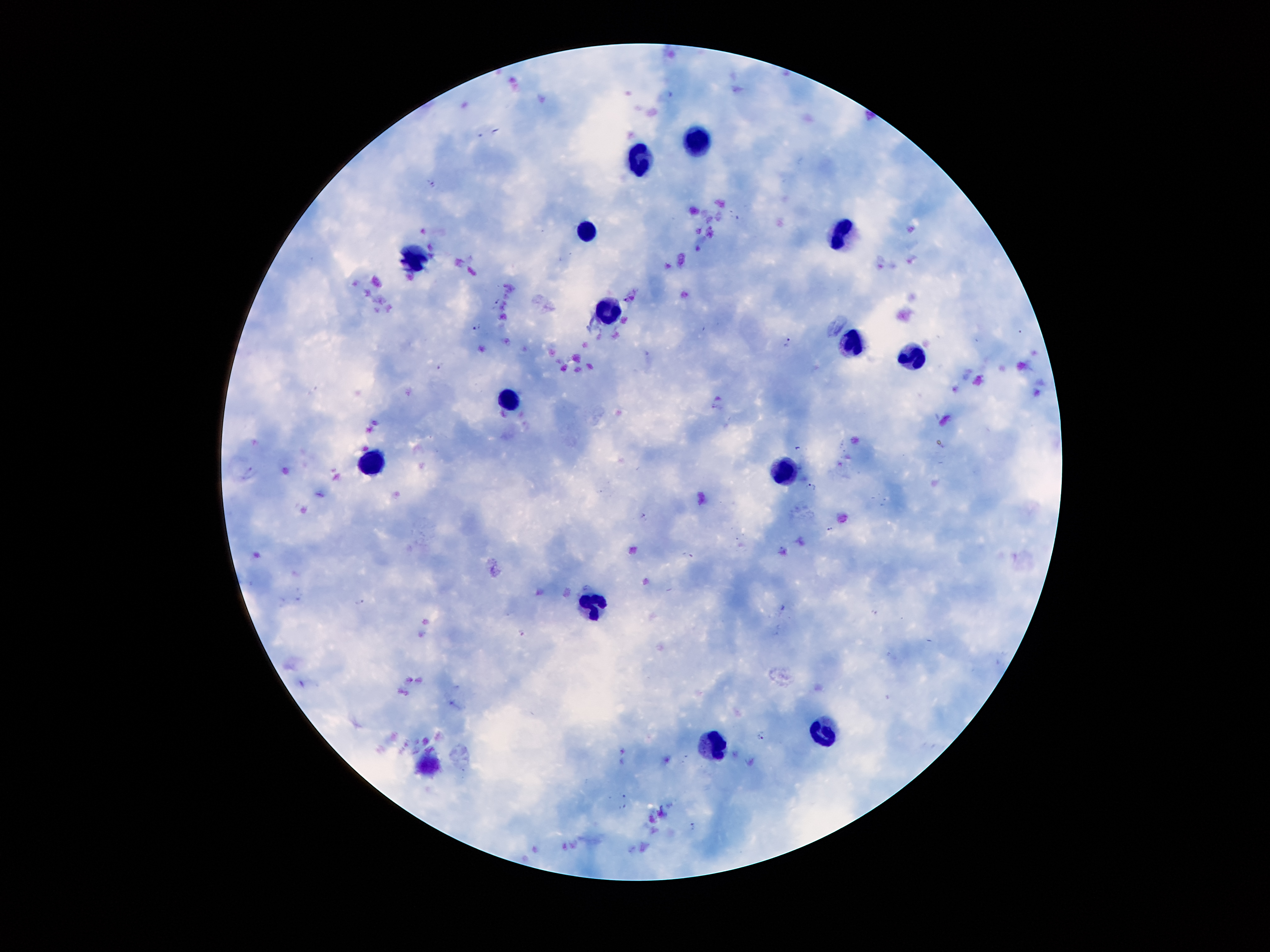
plasmodium_parasite_locations: 'approximate centers as [x, y] in pixels: [432, 182], [477, 328], [790, 342], [442, 367], [716, 407], [810, 487], [644, 516], [831, 530], [362, 604], [522, 634], [761, 736], [692, 827]'
capture: smartphone through the microscope eyepiece
image_size: 1270×952 pixels
stain: Giemsa
magnification: 100x
field_of_view: one from this slide
patient_malaria_status: infected with Plasmodium falciparum
preparation: thick blood smear
leukocyte_locations: 'approximate centers as [x, y] in pixels: [692, 141], [640, 158], [587, 231], [844, 234], [419, 258], [606, 313], [848, 339], [917, 354], [507, 406], [370, 464], [787, 470], [587, 599], [822, 733], [719, 742]'